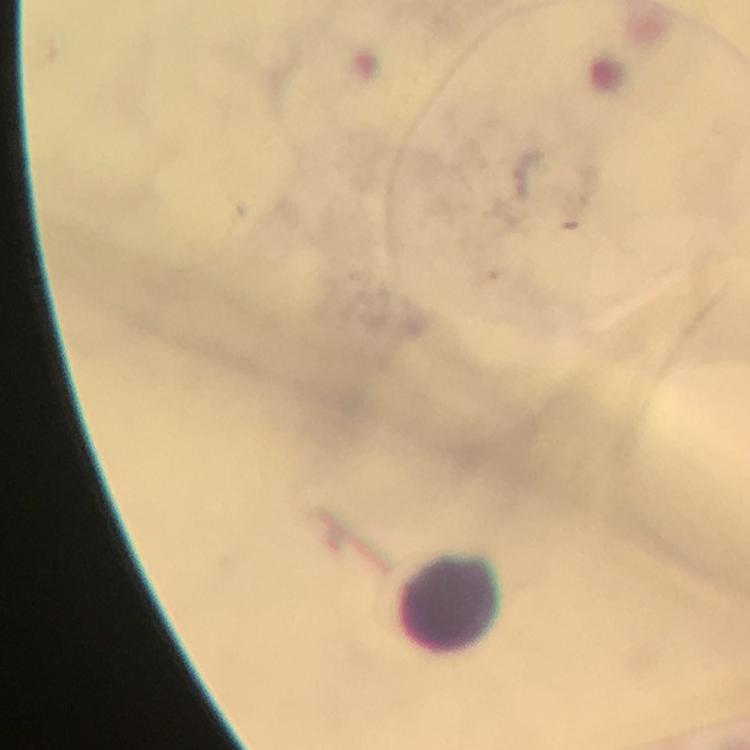 Approximate centers as {x, y} in pixels. Leukocyte locations: {451, 604}. Immersion oil was used. Image is 750×750 pixels. Plasmodium parasites: none seen. Thick blood film. 100x magnification. Cropped region of a single field of view. Photographed through the microscope with a smartphone camera. Giemsa-stained preparation. From a malaria diagnostic workup.